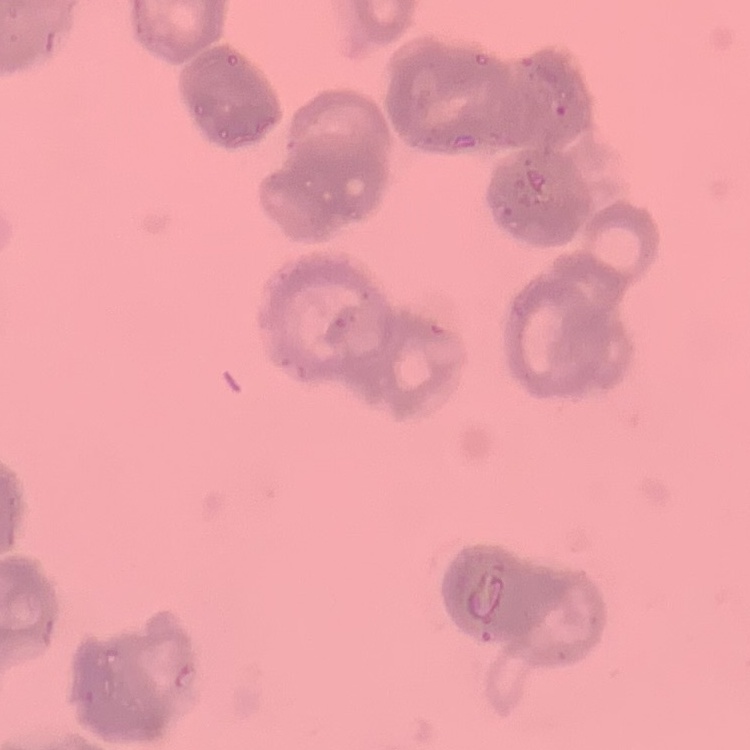

The red blood cells exhibit rouleaux formation. Thin blood smear. Field's or Giemsa stain. Square crop of a larger photomicrograph.